Name the parasite shown.
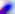

This is Toxoplasma gondii.

Photomicrograph. 400x magnification.